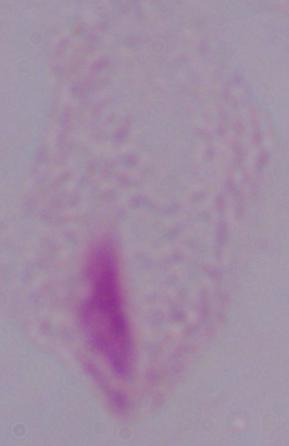
modality = micrograph
identification = trichomonad
magnification = 1000x